Outline every malaria parasite.
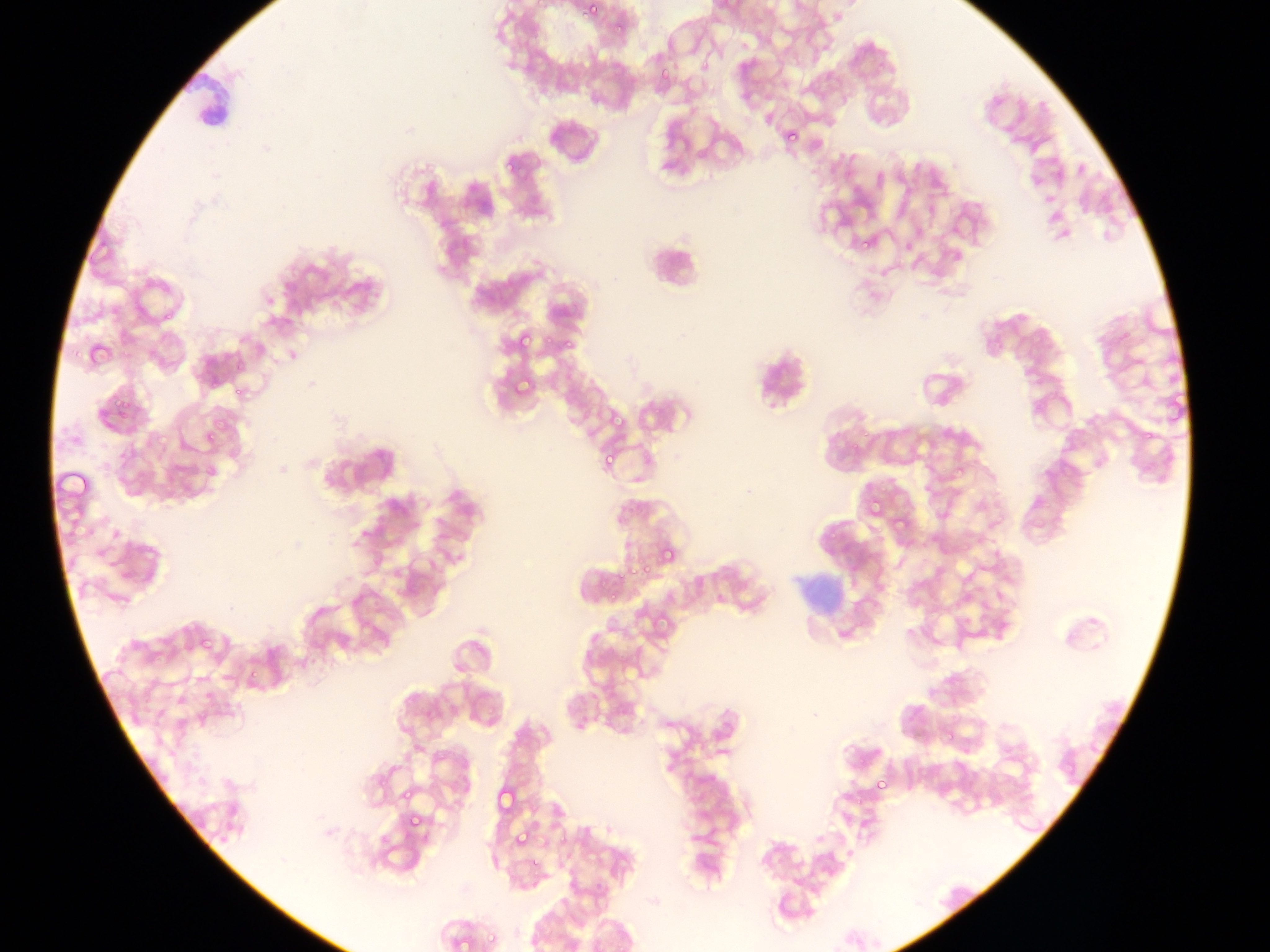
Approximate bounding boxes as (left, top, right, bottom) in pixels.
Malaria parasites: (581, 0, 602, 23), (609, 13, 632, 37), (655, 68, 676, 80), (776, 118, 805, 143), (500, 151, 528, 181), (1073, 161, 1088, 178), (855, 240, 872, 252), (507, 324, 551, 355), (513, 329, 536, 355), (565, 338, 579, 358), (510, 373, 537, 402), (114, 396, 136, 420), (607, 400, 629, 436), (213, 414, 234, 436), (204, 419, 232, 451), (201, 426, 220, 449), (598, 448, 622, 476), (863, 495, 886, 521), (891, 511, 912, 535), (657, 542, 679, 567), (622, 560, 654, 577), (599, 584, 621, 605), (197, 634, 219, 659), (201, 685, 219, 705), (873, 776, 893, 796), (399, 783, 413, 807), (489, 789, 531, 816), (507, 816, 545, 853), (409, 817, 425, 833), (511, 824, 535, 850), (526, 852, 547, 868), (485, 928, 491, 948).

field of view = single
country = Ghana
image size = 1270×952 pixels
capture = mobile-phone photograph through a microscope
preparation = thin blood film